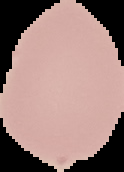

Segmented cell region on a black background. Result: negative for Plasmodium parasites. Image is 124×172 pixels. From a thin blood smear.